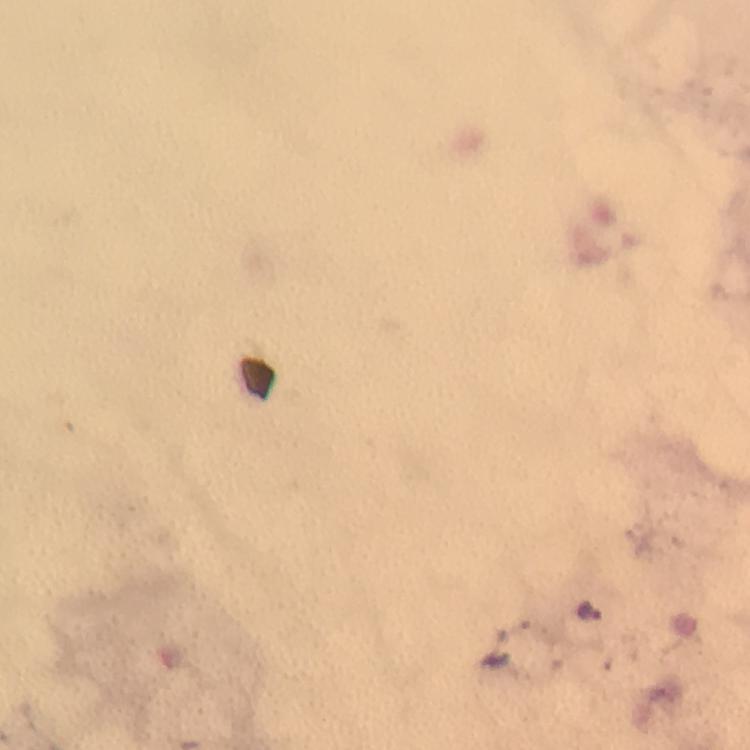
immersion_oil: used
image_size: 750×750 pixels
capture: smartphone photograph through a microscope
malaria_parasite_locations: 'approximate centers as {x, y} in pixels: {594, 611}'
stain: Giemsa
cropped_from: one field of view
magnification: 100x
preparation: thick smear
context: from a malaria diagnostic workup